Outline each Plasmodium falciparum-infected red blood cell.
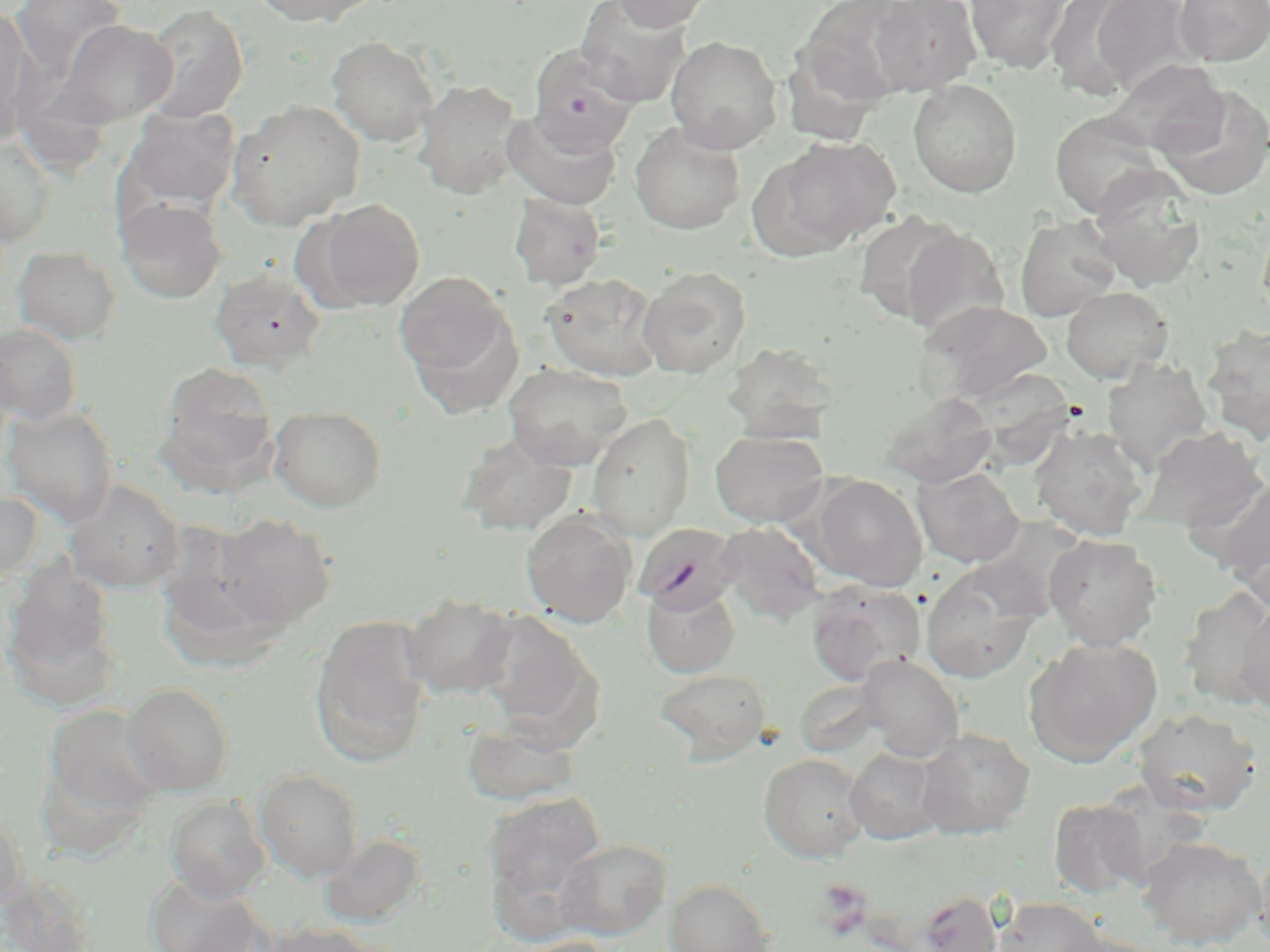

Approximate bounding boxes as (x1,y1)-(x2,y2) corner pairs in pixels.
Plasmodium falciparum-infected red blood cells: (634,524)-(741,614).

Platelet locations: (814,878)-(873,938). Uninfected red blood cell locations: (10,0)-(127,83), (250,0)-(378,27), (612,0)-(717,32), (870,0)-(982,96), (964,0)-(1074,73), (1045,0)-(1156,99), (1086,0)-(1198,94), (1174,0)-(1270,66), (575,1)-(691,105), (795,1)-(919,110), (140,5)-(248,123), (0,9)-(35,140), (50,20)-(178,128), (665,35)-(783,154), (326,36)-(439,147), (527,47)-(638,157), (1101,59)-(1227,155), (415,79)-(523,199), (907,79)-(1023,198), (1155,85)-(1270,200), (227,99)-(365,229), (123,106)-(240,212), (503,110)-(622,210), (1049,111)-(1165,218), (629,123)-(744,234), (760,135)-(900,254), (1,137)-(56,247), (1086,168)-(1207,292), (509,193)-(606,289), (115,197)-(228,304), (316,199)-(423,309), (1014,215)-(1121,321), (1257,216)-(1270,329), (897,225)-(1009,340), (13,246)-(121,344), (637,267)-(751,378), (209,269)-(327,371), (395,271)-(515,393), (542,273)-(665,381), (1061,286)-(1173,383), (920,300)-(1052,405), (0,324)-(83,424), (1201,325)-(1270,443), (723,342)-(839,442), (1102,358)-(1212,473), (503,362)-(632,469), (157,363)-(280,487), (879,390)-(997,488), (1,406)-(118,526), (268,406)-(387,513), (587,413)-(695,539), (1030,424)-(1148,541), (1134,426)-(1267,532), (709,430)-(829,528), (456,433)-(578,536), (912,466)-(1024,567), (1192,470)-(1270,588), (807,474)-(928,590), (64,479)-(185,592), (0,491)-(43,585), (1222,491)-(1270,608), (521,510)-(636,627), (213,513)-(336,628), (715,522)-(825,624), (1043,533)-(1163,650), (919,562)-(1044,683), (806,582)-(926,686), (642,583)-(740,678), (1179,589)-(1270,709), (401,594)-(518,699), (1236,601)-(1270,716), (475,611)-(600,740), (309,616)-(433,768), (1024,636)-(1161,766), (858,654)-(963,761), (653,667)-(772,765), (121,682)-(235,795), (41,702)-(165,825), (1132,708)-(1263,816), (460,720)-(582,806), (917,727)-(1035,838), (845,746)-(948,844), (758,753)-(871,862), (255,769)-(364,882), (484,791)-(607,923), (166,797)-(270,902), (1049,798)-(1150,898), (0,808)-(27,914), (320,833)-(427,927), (1138,836)-(1266,948), (555,838)-(671,940), (1253,843)-(1270,952), (0,870)-(98,952), (143,873)-(270,952), (665,877)-(776,952), (915,890)-(1004,952), (994,896)-(1105,952), (259,921)-(382,952), (1051,931)-(1168,952), (504,936)-(621,952). Slide-level diagnosis: Plasmodium falciparum. May-Grünwald-Giemsa stain. Captured at 1000x magnification. Single field of view. Light microscopy. Thin blood smear. Image is 1270×952 pixels.